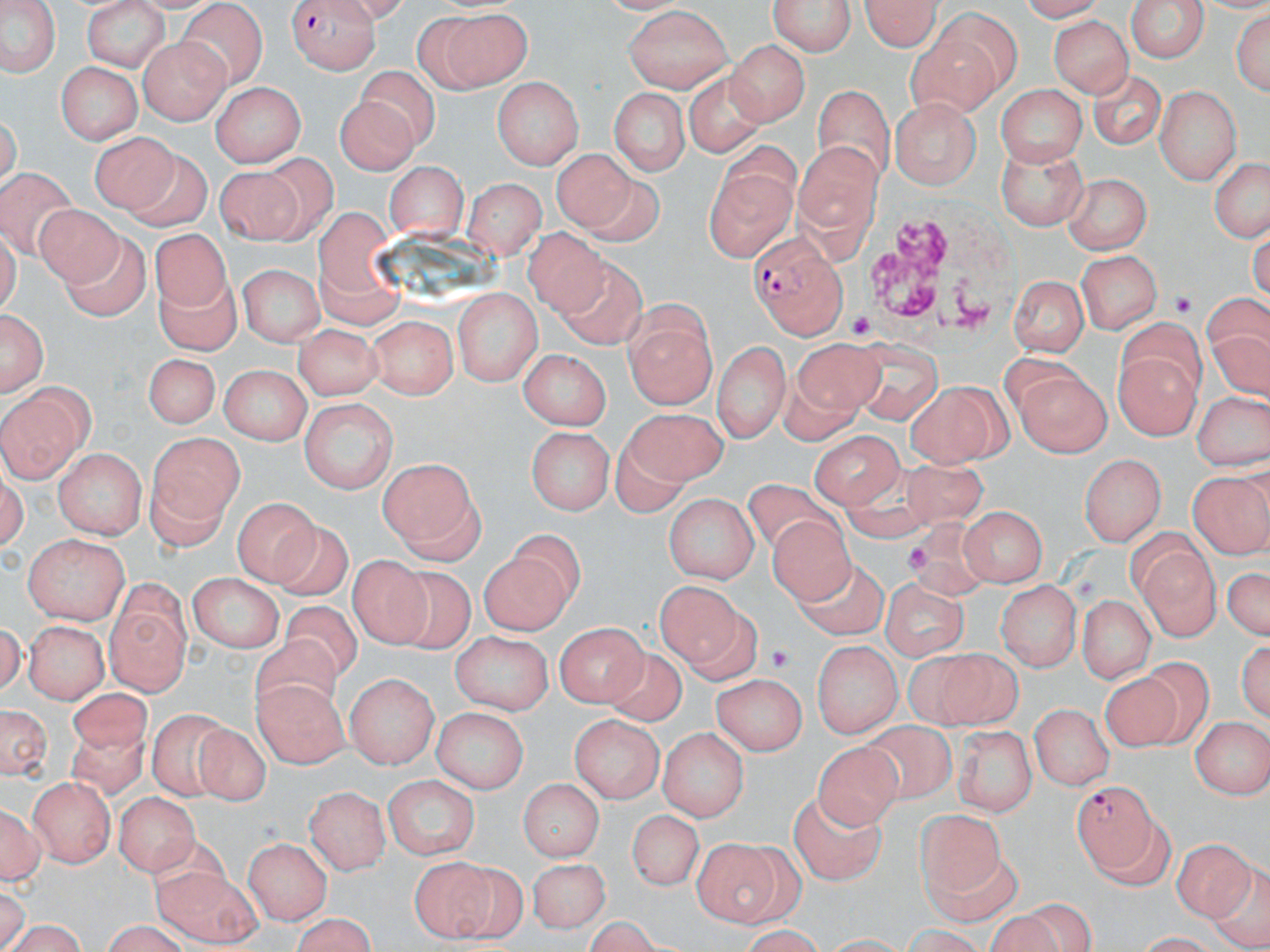

Summary:
  - Coordinate format: approximate bounding boxes as named x1/y1/x2/y2 corners in pixels
  - White blood cell locations: (x1=861, y1=197, x2=1018, y2=354)
  - Plasmodium falciparum-infected red blood cell locations: (x1=288, y1=0, x2=382, y2=71), (x1=751, y1=232, x2=848, y2=341), (x1=1072, y1=780, x2=1162, y2=877)
  - Platelet locations: (x1=1169, y1=289, x2=1199, y2=316), (x1=847, y1=312, x2=875, y2=339), (x1=904, y1=541, x2=932, y2=577), (x1=766, y1=642, x2=792, y2=670)
  - Uninfected red blood cell locations: (x1=858, y1=0, x2=941, y2=52), (x1=1124, y1=0, x2=1211, y2=63), (x1=2, y1=1, x2=56, y2=77), (x1=772, y1=1, x2=855, y2=56), (x1=82, y1=3, x2=176, y2=71), (x1=622, y1=6, x2=731, y2=94), (x1=421, y1=8, x2=534, y2=95), (x1=1234, y1=9, x2=1268, y2=102), (x1=175, y1=11, x2=263, y2=95), (x1=1052, y1=18, x2=1134, y2=97), (x1=904, y1=33, x2=1004, y2=115), (x1=136, y1=35, x2=231, y2=121), (x1=727, y1=40, x2=806, y2=125), (x1=56, y1=62, x2=139, y2=143), (x1=1087, y1=66, x2=1165, y2=149), (x1=338, y1=67, x2=440, y2=171), (x1=674, y1=69, x2=775, y2=153), (x1=493, y1=76, x2=582, y2=169), (x1=997, y1=80, x2=1085, y2=168), (x1=211, y1=81, x2=306, y2=169), (x1=814, y1=84, x2=893, y2=185), (x1=1155, y1=85, x2=1241, y2=184), (x1=613, y1=87, x2=686, y2=177), (x1=892, y1=99, x2=982, y2=189), (x1=91, y1=134, x2=179, y2=216), (x1=794, y1=139, x2=884, y2=235), (x1=996, y1=148, x2=1088, y2=226), (x1=123, y1=152, x2=212, y2=230), (x1=557, y1=152, x2=642, y2=234), (x1=1207, y1=154, x2=1270, y2=244), (x1=257, y1=156, x2=331, y2=244), (x1=388, y1=161, x2=464, y2=242), (x1=2, y1=167, x2=74, y2=255), (x1=707, y1=167, x2=796, y2=264), (x1=215, y1=169, x2=304, y2=247), (x1=1062, y1=173, x2=1150, y2=253), (x1=469, y1=176, x2=545, y2=259), (x1=29, y1=201, x2=124, y2=289), (x1=315, y1=208, x2=382, y2=311), (x1=520, y1=230, x2=613, y2=321), (x1=72, y1=233, x2=149, y2=315), (x1=156, y1=235, x2=235, y2=311), (x1=1077, y1=249, x2=1160, y2=336), (x1=560, y1=250, x2=647, y2=349), (x1=235, y1=262, x2=325, y2=348), (x1=1006, y1=268, x2=1089, y2=354), (x1=151, y1=275, x2=238, y2=355), (x1=452, y1=289, x2=539, y2=386), (x1=1210, y1=291, x2=1270, y2=392), (x1=2, y1=307, x2=47, y2=396), (x1=625, y1=311, x2=716, y2=408), (x1=367, y1=314, x2=458, y2=400), (x1=1116, y1=324, x2=1206, y2=436), (x1=295, y1=325, x2=380, y2=395), (x1=713, y1=338, x2=789, y2=447), (x1=852, y1=338, x2=941, y2=425), (x1=797, y1=341, x2=883, y2=411), (x1=519, y1=348, x2=610, y2=429), (x1=142, y1=353, x2=217, y2=430), (x1=1013, y1=364, x2=1110, y2=456), (x1=219, y1=365, x2=308, y2=447), (x1=905, y1=380, x2=1010, y2=467), (x1=1191, y1=392, x2=1268, y2=471), (x1=2, y1=397, x2=80, y2=478), (x1=299, y1=399, x2=394, y2=494), (x1=621, y1=412, x2=726, y2=488), (x1=527, y1=425, x2=617, y2=514), (x1=812, y1=429, x2=904, y2=509), (x1=143, y1=433, x2=242, y2=533), (x1=51, y1=448, x2=148, y2=537), (x1=1079, y1=453, x2=1165, y2=549), (x1=376, y1=456, x2=484, y2=557), (x1=900, y1=462, x2=997, y2=529), (x1=1187, y1=469, x2=1269, y2=556), (x1=735, y1=482, x2=848, y2=553), (x1=665, y1=494, x2=758, y2=582), (x1=233, y1=497, x2=319, y2=581), (x1=958, y1=505, x2=1044, y2=585), (x1=764, y1=514, x2=851, y2=605), (x1=895, y1=518, x2=993, y2=598), (x1=266, y1=519, x2=350, y2=601), (x1=506, y1=528, x2=587, y2=611), (x1=22, y1=534, x2=128, y2=624), (x1=1134, y1=544, x2=1219, y2=643), (x1=345, y1=551, x2=431, y2=647), (x1=477, y1=555, x2=572, y2=635), (x1=1222, y1=558, x2=1267, y2=646), (x1=795, y1=563, x2=892, y2=643), (x1=380, y1=564, x2=479, y2=655), (x1=188, y1=575, x2=284, y2=652), (x1=878, y1=578, x2=970, y2=655), (x1=659, y1=579, x2=746, y2=676), (x1=995, y1=579, x2=1080, y2=672), (x1=1073, y1=593, x2=1157, y2=681), (x1=95, y1=600, x2=200, y2=696), (x1=278, y1=600, x2=367, y2=684), (x1=555, y1=618, x2=648, y2=707), (x1=24, y1=620, x2=107, y2=707), (x1=450, y1=631, x2=551, y2=714), (x1=249, y1=632, x2=341, y2=714), (x1=1237, y1=636, x2=1270, y2=723), (x1=813, y1=639, x2=904, y2=738), (x1=601, y1=645, x2=690, y2=723), (x1=928, y1=652, x2=1018, y2=727), (x1=714, y1=672, x2=808, y2=756), (x1=344, y1=673, x2=436, y2=770), (x1=1108, y1=678, x2=1184, y2=756), (x1=252, y1=684, x2=353, y2=773), (x1=68, y1=689, x2=154, y2=756), (x1=0, y1=701, x2=51, y2=783), (x1=1026, y1=703, x2=1111, y2=791), (x1=429, y1=707, x2=528, y2=793), (x1=143, y1=710, x2=244, y2=798), (x1=1189, y1=713, x2=1268, y2=799), (x1=569, y1=714, x2=664, y2=803), (x1=195, y1=721, x2=268, y2=805), (x1=855, y1=721, x2=960, y2=798), (x1=954, y1=724, x2=1036, y2=818), (x1=57, y1=727, x2=154, y2=803), (x1=659, y1=727, x2=747, y2=821), (x1=805, y1=743, x2=904, y2=838), (x1=29, y1=774, x2=116, y2=867), (x1=382, y1=776, x2=480, y2=858), (x1=516, y1=777, x2=602, y2=859), (x1=306, y1=785, x2=391, y2=873), (x1=794, y1=787, x2=883, y2=885), (x1=113, y1=791, x2=199, y2=878), (x1=258, y1=804, x2=365, y2=915), (x1=0, y1=805, x2=44, y2=885), (x1=629, y1=805, x2=705, y2=889), (x1=917, y1=811, x2=1010, y2=906), (x1=1174, y1=829, x2=1261, y2=922), (x1=245, y1=835, x2=335, y2=926), (x1=688, y1=836, x2=799, y2=929), (x1=411, y1=856, x2=496, y2=943), (x1=529, y1=859, x2=608, y2=930), (x1=449, y1=861, x2=529, y2=950), (x1=149, y1=864, x2=266, y2=948), (x1=1025, y1=902, x2=1089, y2=945), (x1=294, y1=912, x2=377, y2=952), (x1=90, y1=919, x2=189, y2=949)
  - Slide-level diagnosis: Plasmodium falciparum
  - Preparation: thin blood smear
  - Modality: optical microscopy
  - Field of view: one of a larger specimen
  - Stain: May-Grünwald-Giemsa
  - Magnification: 1000x
  - Image size: 1270×952 pixels